Assess this cell for malaria.
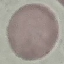
Uninfected.

Cell patch, automatically extracted from a larger field of view and resized to 64 × 64 pixels. Thin blood smear. Photographed with a smartphone camera at the microscope eyepiece. Giemsa stain.